Assess this cell for malaria.
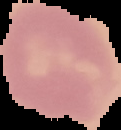
Uninfected.

image size = 121×130 pixels
preparation = thin blood smear
image type = segmented cell region with the area outside set to black